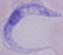

Summary:
  - Identification: trypanosome
  - Magnification: 1000x
  - Modality: photomicrograph